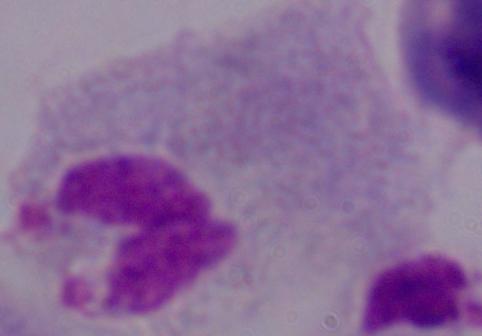

magnification = 1000x
modality = photomicrograph
identification = trichomonad